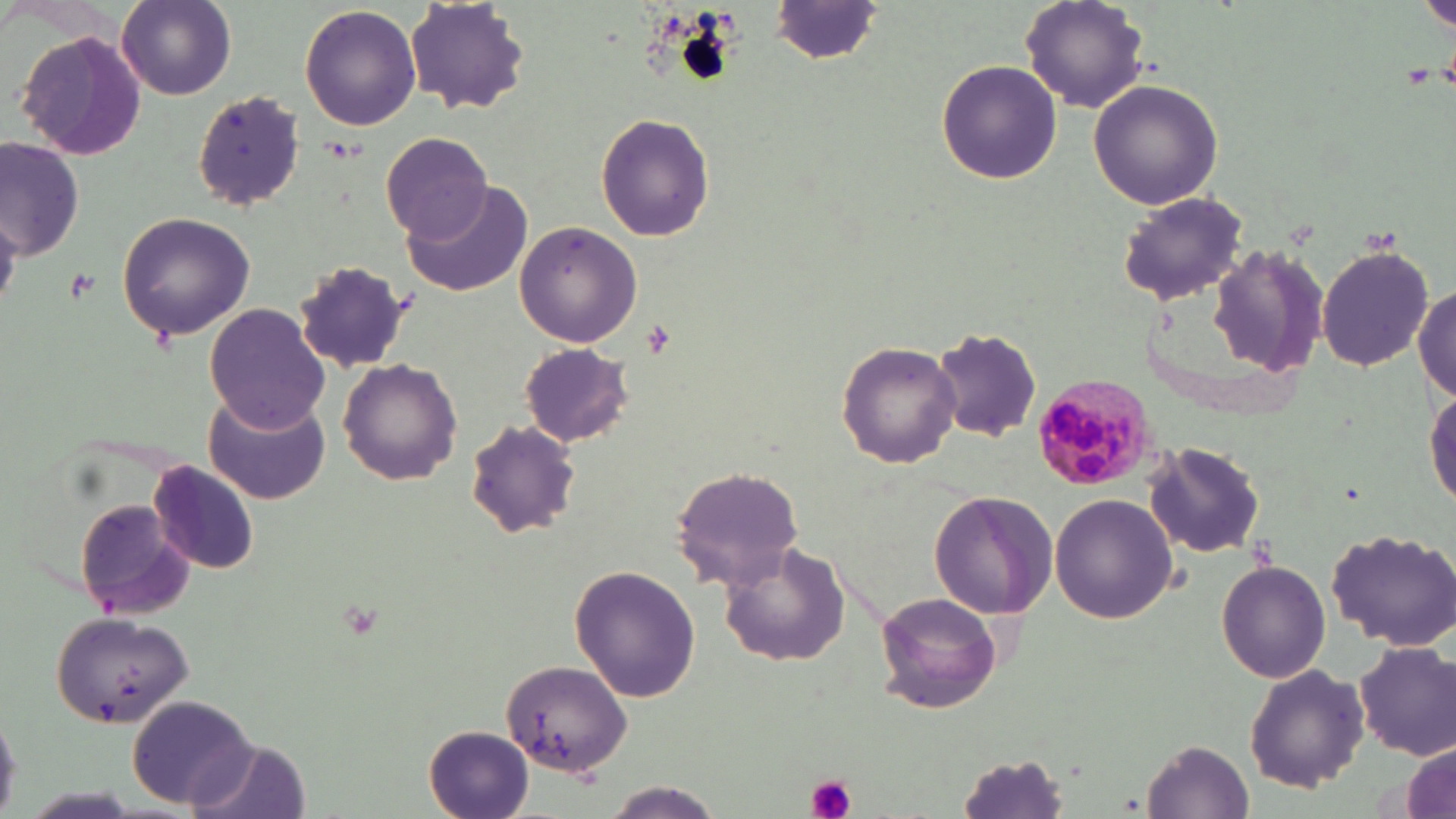
{
  "plasmodium_malariae_infected_red_blood_cell_locations": "approximate bounding boxes as [x1, y1, x2, y2] in pixels: [1035, 375, 1152, 490]",
  "slide_level_diagnosis": "Plasmodium malariae",
  "preparation": "thin blood film",
  "image_size": "1456×819 pixels",
  "stain": "May-Grünwald-Giemsa",
  "modality": "optical microscopy",
  "uninfected_red_blood_cell_locations": "approximate bounding boxes as [x1, y1, x2, y2] in pixels: [116, 0, 236, 100], [770, 0, 885, 64], [1020, 0, 1148, 112], [1422, 0, 1456, 32], [407, 1, 530, 114], [299, 4, 422, 132], [15, 27, 149, 162], [935, 59, 1062, 184], [1088, 78, 1224, 210], [192, 91, 305, 211], [595, 112, 716, 242], [381, 130, 491, 240], [2, 141, 86, 263], [402, 180, 531, 295], [1117, 192, 1251, 305], [116, 210, 256, 340], [513, 220, 643, 348], [1318, 245, 1432, 372], [1203, 248, 1330, 378], [279, 265, 416, 386], [1413, 286, 1455, 404], [203, 301, 333, 431], [931, 326, 1044, 443], [837, 340, 962, 468], [519, 342, 633, 447], [337, 357, 462, 485], [1426, 384, 1455, 513], [201, 390, 330, 505], [464, 419, 584, 540], [1144, 440, 1267, 559], [147, 462, 261, 575], [669, 465, 808, 590], [927, 490, 1059, 619], [1050, 495, 1178, 624], [73, 498, 198, 619], [1324, 527, 1456, 649], [718, 540, 851, 668], [1214, 559, 1332, 683], [568, 566, 700, 703], [872, 590, 1003, 713], [47, 611, 192, 729], [1353, 640, 1456, 760], [500, 660, 630, 776], [1244, 662, 1370, 793], [126, 694, 258, 809], [0, 708, 26, 811], [423, 725, 536, 819], [1400, 734, 1455, 819], [187, 735, 313, 819], [1146, 739, 1252, 816], [953, 752, 1074, 819], [603, 782, 726, 818]",
  "platelet_locations": "approximate bounding boxes as [x1, y1, x2, y2] in pixels: [63, 271, 98, 304], [805, 774, 857, 819]",
  "field_of_view": "single",
  "magnification": "1000x"
}